Locate every blood parasite and identify its species.
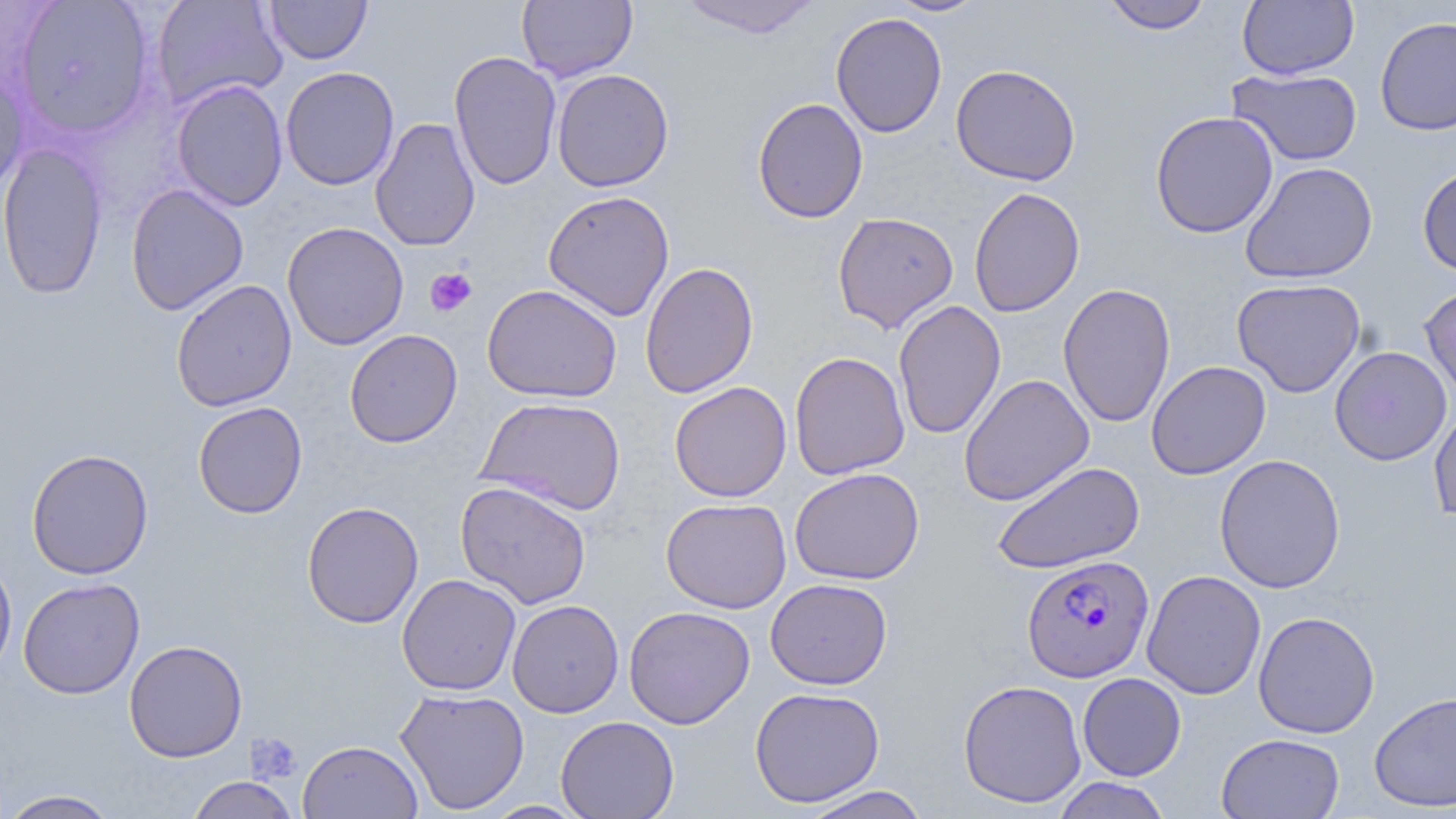

Approximate bounding boxes as [x1, y1, x2, y2] in pixels.
Plasmodium falciparum-infected red blood cells: [1021, 554, 1154, 683].
No Plasmodium ovale, Plasmodium malariae, Plasmodium vivax, Babesia divergens, or Trypanosoma brucei observed.

Summary:
  - Platelet locations: [425, 267, 478, 317], [246, 732, 302, 784]
  - Uninfected red blood cell locations: [14, 0, 156, 139], [151, 0, 288, 111], [517, 0, 638, 83], [676, 0, 824, 38], [886, 0, 989, 17], [1100, 0, 1214, 34], [1237, 0, 1359, 80], [264, 1, 373, 65], [830, 12, 947, 138], [1375, 15, 1456, 136], [448, 51, 562, 191], [950, 63, 1081, 186], [280, 66, 400, 191], [0, 67, 30, 196], [1227, 68, 1363, 167], [551, 69, 675, 192], [171, 79, 288, 211], [751, 97, 868, 224], [1150, 110, 1278, 239], [370, 117, 481, 252], [0, 142, 108, 301], [1239, 161, 1378, 284], [1417, 163, 1456, 277], [125, 184, 249, 316], [968, 187, 1086, 318], [542, 190, 675, 321], [832, 212, 959, 333], [282, 221, 409, 350], [639, 261, 759, 399], [1231, 278, 1366, 398], [171, 279, 297, 411], [1058, 282, 1176, 429], [1419, 282, 1456, 403], [482, 284, 622, 404], [893, 299, 1006, 440], [344, 329, 463, 448], [1330, 345, 1452, 466], [789, 351, 910, 480], [1146, 360, 1271, 480], [958, 373, 1094, 506], [669, 381, 792, 503], [476, 396, 626, 515], [193, 401, 308, 519], [1429, 404, 1456, 526], [26, 448, 154, 580], [1214, 454, 1346, 594], [991, 460, 1145, 575], [789, 467, 924, 585], [455, 480, 592, 609], [661, 498, 792, 613], [301, 501, 424, 628], [0, 554, 17, 681], [1141, 570, 1266, 700], [397, 574, 522, 696], [18, 577, 145, 699], [764, 578, 893, 690], [507, 599, 624, 718], [623, 605, 755, 729], [1253, 610, 1380, 739], [124, 639, 248, 762], [1077, 672, 1186, 780], [958, 679, 1087, 808], [749, 686, 885, 807], [394, 687, 530, 815], [1369, 690, 1456, 812], [555, 715, 679, 819], [1216, 732, 1345, 818], [298, 740, 423, 819], [185, 776, 300, 819], [1051, 777, 1173, 819], [800, 785, 932, 819], [1, 789, 122, 819], [483, 800, 588, 818]
  - Slide-level diagnosis: Plasmodium falciparum
  - Image size: 1456×819 pixels
  - Stain: May-Grünwald-Giemsa
  - Field of view: single
  - Preparation: thin blood smear
  - Magnification: 1000x
  - Modality: light microscopy